State the preparation type.
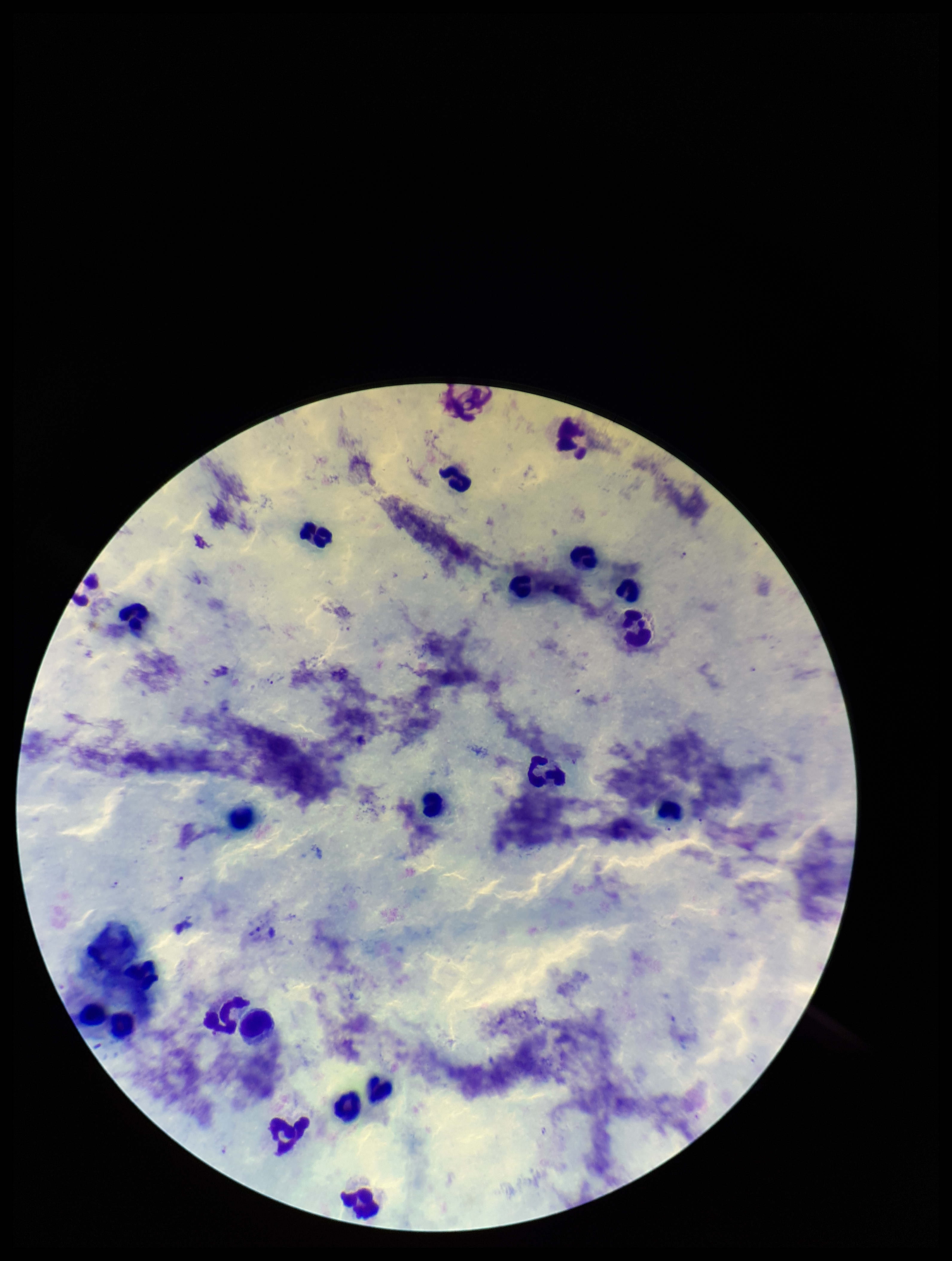

Thick.

species_reported_for_this_patient: Plasmodium falciparum
plasmodium_parasites: seen
field_of_view: one from this slide
image_size: 952×1261 pixels
capture: smartphone photograph through the microscope eyepiece
stain: Giemsa
patient_malaria_status: infected
leukocyte_count: 23
parasite_count: 4